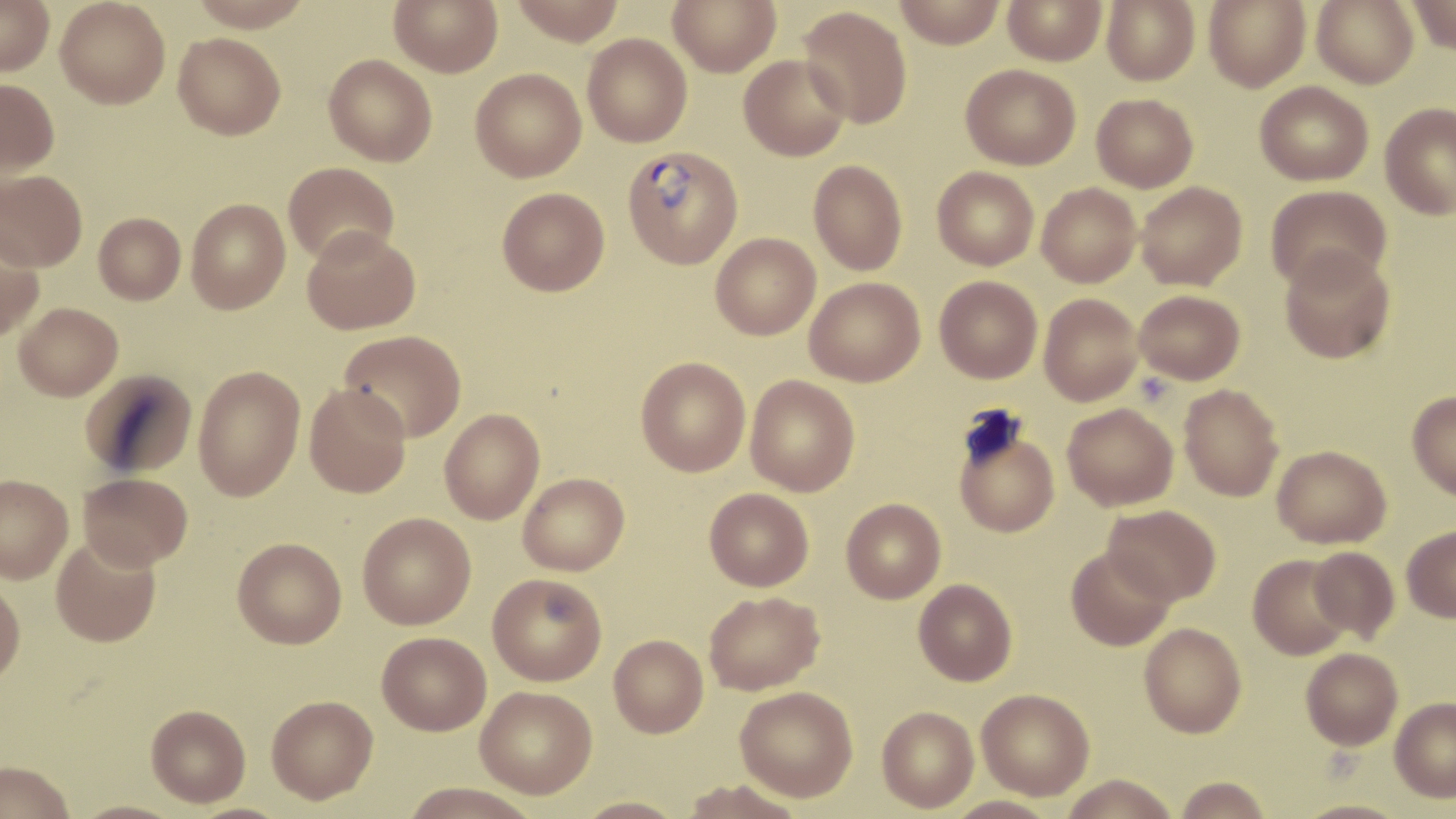

Approximate bounding boxes as named x1/y1/x2/y2 corners in pixels. Uninfected red blood cell locations: (x1=0, y1=0, x2=54, y2=75), (x1=55, y1=0, x2=170, y2=109), (x1=187, y1=0, x2=316, y2=31), (x1=389, y1=0, x2=503, y2=77), (x1=510, y1=0, x2=626, y2=45), (x1=668, y1=0, x2=780, y2=76), (x1=893, y1=0, x2=1006, y2=48), (x1=1002, y1=0, x2=1107, y2=66), (x1=1204, y1=0, x2=1311, y2=92), (x1=1311, y1=0, x2=1419, y2=88), (x1=1405, y1=0, x2=1455, y2=54), (x1=1102, y1=1, x2=1200, y2=85), (x1=798, y1=5, x2=912, y2=129), (x1=173, y1=32, x2=286, y2=140), (x1=582, y1=33, x2=692, y2=147), (x1=324, y1=54, x2=437, y2=166), (x1=738, y1=55, x2=850, y2=161), (x1=961, y1=63, x2=1081, y2=170), (x1=470, y1=68, x2=586, y2=182), (x1=0, y1=79, x2=59, y2=176), (x1=1255, y1=81, x2=1373, y2=185), (x1=1091, y1=93, x2=1198, y2=192), (x1=1380, y1=103, x2=1456, y2=220), (x1=808, y1=160, x2=908, y2=276), (x1=283, y1=162, x2=399, y2=265), (x1=932, y1=166, x2=1039, y2=270), (x1=0, y1=170, x2=88, y2=271), (x1=1136, y1=181, x2=1248, y2=291), (x1=1037, y1=182, x2=1141, y2=287), (x1=1266, y1=185, x2=1391, y2=293), (x1=497, y1=187, x2=610, y2=296), (x1=186, y1=198, x2=290, y2=314), (x1=93, y1=212, x2=185, y2=304), (x1=302, y1=226, x2=421, y2=334), (x1=0, y1=231, x2=44, y2=341), (x1=710, y1=233, x2=821, y2=340), (x1=1280, y1=247, x2=1395, y2=363), (x1=935, y1=276, x2=1042, y2=383), (x1=804, y1=277, x2=925, y2=387), (x1=1134, y1=289, x2=1245, y2=385), (x1=1039, y1=293, x2=1143, y2=406), (x1=13, y1=302, x2=123, y2=400), (x1=340, y1=329, x2=467, y2=443), (x1=636, y1=357, x2=750, y2=476), (x1=192, y1=364, x2=305, y2=501), (x1=80, y1=369, x2=198, y2=478), (x1=745, y1=375, x2=860, y2=496), (x1=304, y1=383, x2=412, y2=498), (x1=1178, y1=383, x2=1284, y2=502), (x1=1407, y1=391, x2=1456, y2=500), (x1=1063, y1=403, x2=1178, y2=511), (x1=439, y1=408, x2=544, y2=524), (x1=953, y1=420, x2=1059, y2=538), (x1=1272, y1=445, x2=1391, y2=548), (x1=78, y1=472, x2=193, y2=571), (x1=518, y1=472, x2=629, y2=575), (x1=0, y1=474, x2=73, y2=583), (x1=704, y1=488, x2=814, y2=591), (x1=841, y1=498, x2=946, y2=603), (x1=1102, y1=504, x2=1221, y2=605), (x1=357, y1=512, x2=476, y2=629), (x1=1401, y1=525, x2=1456, y2=622), (x1=51, y1=535, x2=162, y2=647), (x1=232, y1=537, x2=346, y2=648), (x1=1066, y1=546, x2=1176, y2=651), (x1=1307, y1=546, x2=1399, y2=642), (x1=1248, y1=554, x2=1355, y2=660), (x1=488, y1=573, x2=607, y2=685), (x1=914, y1=578, x2=1017, y2=686), (x1=0, y1=579, x2=25, y2=689), (x1=704, y1=591, x2=824, y2=695), (x1=1139, y1=622, x2=1247, y2=738), (x1=376, y1=631, x2=491, y2=735), (x1=608, y1=634, x2=708, y2=737), (x1=1301, y1=647, x2=1403, y2=750), (x1=475, y1=686, x2=597, y2=799), (x1=734, y1=686, x2=858, y2=802), (x1=977, y1=688, x2=1094, y2=800), (x1=266, y1=695, x2=378, y2=804), (x1=1390, y1=698, x2=1456, y2=802), (x1=146, y1=704, x2=251, y2=807), (x1=877, y1=706, x2=979, y2=813), (x1=0, y1=761, x2=75, y2=819), (x1=1059, y1=773, x2=1181, y2=818), (x1=1173, y1=776, x2=1274, y2=818), (x1=681, y1=778, x2=808, y2=818), (x1=397, y1=782, x2=544, y2=818), (x1=945, y1=795, x2=1059, y2=819), (x1=574, y1=796, x2=690, y2=819), (x1=1295, y1=798, x2=1409, y2=819), (x1=70, y1=799, x2=186, y2=819). Plasmodium vivax-infected red blood cell locations: (x1=622, y1=144, x2=743, y2=269). Slide-level diagnosis: Plasmodium vivax. One field of a larger specimen. Light microscopy. Captured at 1000x magnification. Image is 1456×819 pixels. Thin blood film. May-Grünwald-Giemsa stain.